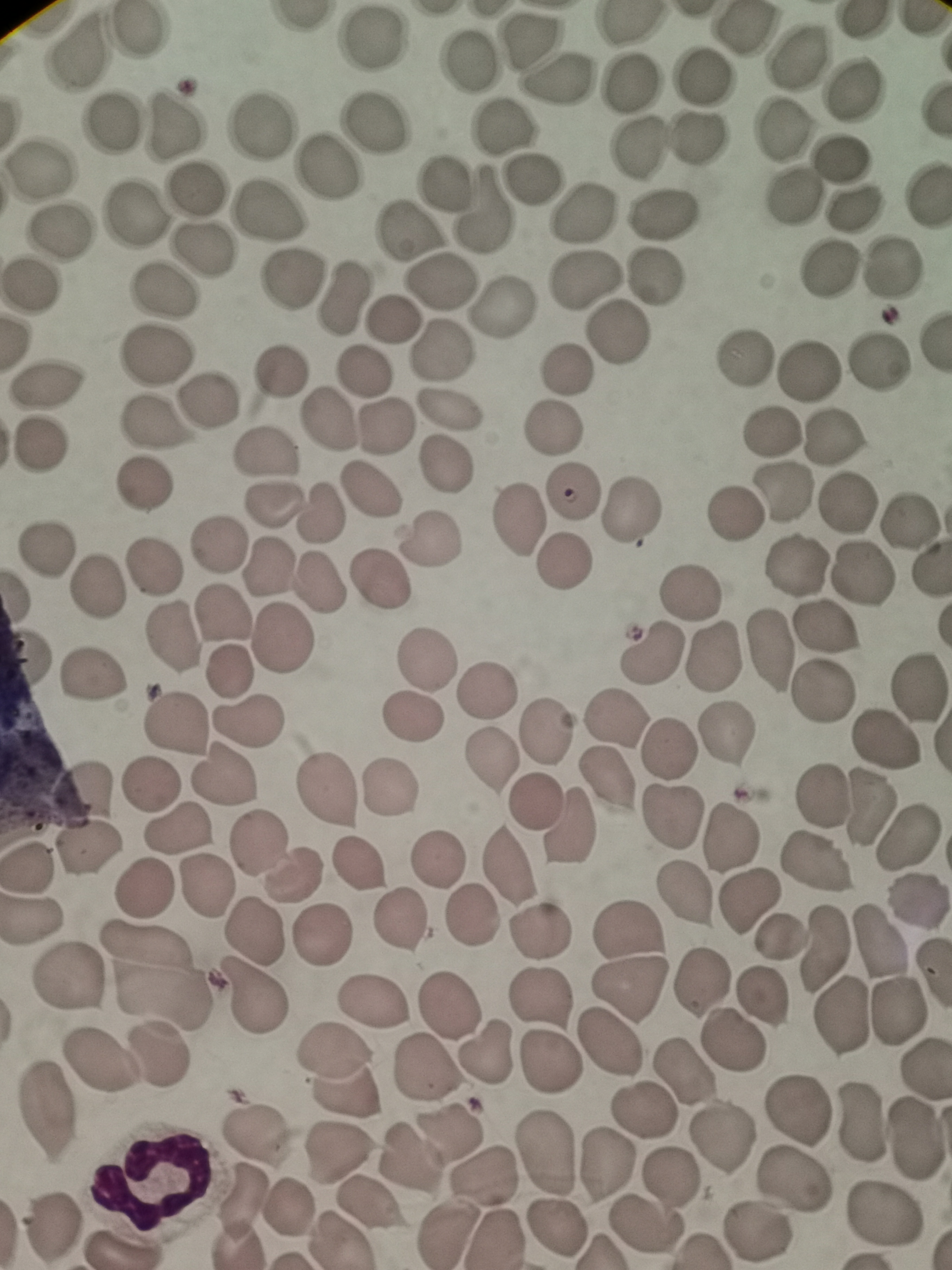
Approximate centers as [x, y] in pixels.
Summary:
  - Cell locations: [136, 31], [742, 31], [531, 38], [371, 39], [77, 53], [798, 59], [468, 63], [702, 79], [556, 81], [629, 81], [853, 92], [111, 119], [379, 123], [175, 124], [259, 125], [503, 130], [783, 131], [699, 135], [639, 148], [842, 157], [328, 168], [39, 169], [441, 181], [532, 182], [196, 188], [927, 194], [791, 200], [482, 210], [854, 210], [268, 211], [667, 214], [134, 216], [583, 216], [60, 230], [404, 231], [202, 249], [888, 269], [825, 272], [655, 276], [290, 278], [585, 281], [440, 282], [30, 287], [163, 292], [340, 296], [504, 308], [391, 320], [619, 331], [441, 350], [744, 356], [153, 357], [878, 360], [362, 370], [564, 370], [808, 371], [279, 373], [47, 385], [208, 401], [446, 408], [326, 419], [152, 422], [385, 428], [553, 429], [771, 431], [835, 439], [41, 447], [264, 454], [444, 462], [143, 483], [368, 488], [571, 492], [785, 494], [273, 505], [847, 506], [631, 510], [734, 513], [318, 514], [910, 519], [517, 520], [432, 539], [218, 545], [44, 547], [562, 560], [267, 564], [796, 565], [155, 566], [861, 574], [322, 580], [379, 580], [95, 588], [688, 591], [220, 611], [281, 637], [170, 638], [773, 653], [654, 654], [714, 658], [425, 661], [226, 671], [93, 676], [916, 687], [485, 690], [822, 693], [410, 719], [615, 719], [177, 722], [248, 723], [549, 728], [729, 733], [884, 739], [669, 749], [491, 763], [223, 775], [604, 781], [149, 784], [324, 790], [387, 790], [86, 791], [821, 798], [534, 800], [870, 806], [670, 817], [570, 828], [178, 829], [730, 835], [907, 839], [258, 844], [86, 851], [437, 857], [819, 863], [355, 864], [504, 866], [27, 867], [292, 875], [206, 887], [143, 888], [684, 894], [749, 902], [914, 903], [473, 916], [400, 920], [33, 924], [253, 930], [630, 931], [539, 932], [320, 935], [781, 938], [880, 941], [825, 948], [154, 975], [66, 979], [702, 984], [631, 988], [762, 996], [539, 997], [252, 999], [374, 1003], [449, 1005], [901, 1013], [842, 1017], [731, 1040], [611, 1043], [486, 1052], [160, 1055], [99, 1061], [547, 1063], [427, 1066], [339, 1069], [685, 1072], [48, 1107], [799, 1109], [645, 1111], [862, 1121], [449, 1132], [256, 1133], [722, 1136], [916, 1139], [343, 1154], [546, 1154], [409, 1157], [609, 1164], [485, 1176], [670, 1181], [795, 1181], [240, 1203], [370, 1204], [289, 1208], [882, 1215], [647, 1227], [50, 1229], [557, 1229], [755, 1232], [446, 1233], [125, 1248]
  - Image size: 952×1270 pixels
  - Capture: smartphone through the microscope eyepiece
  - Stain: Giemsa
  - Preparation: thin blood smear
  - Field of view: single